Report the malaria status of this cell.
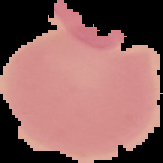
It is uninfected.

From a thin blood smear. The area outside the segmented cell region is set to black. Image is 163×163 pixels.